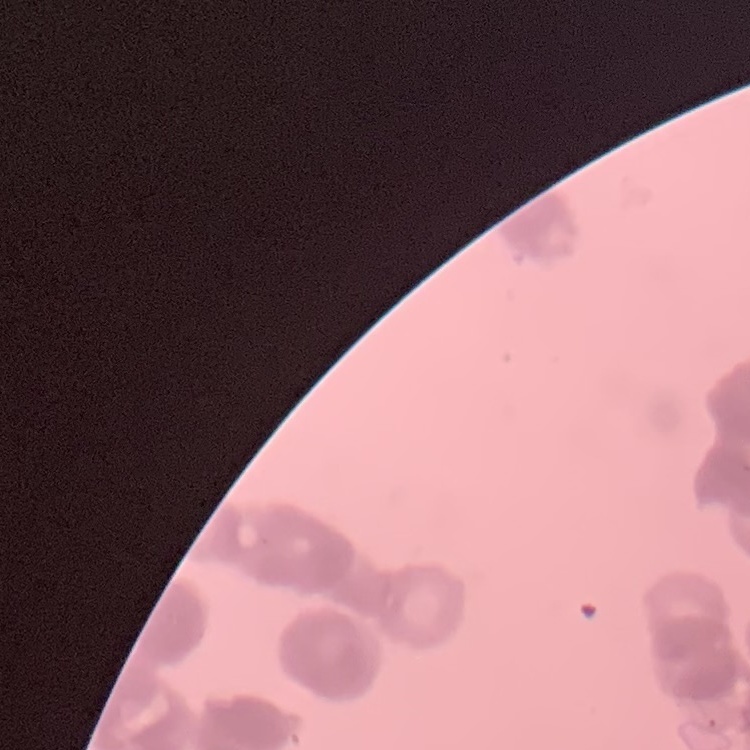
Summary:
  - Red blood cell morphology: rouleaux formation
  - Stain: Field's or Giemsa
  - Preparation: thin blood smear
  - Image type: one tile cut from a larger photomicrograph